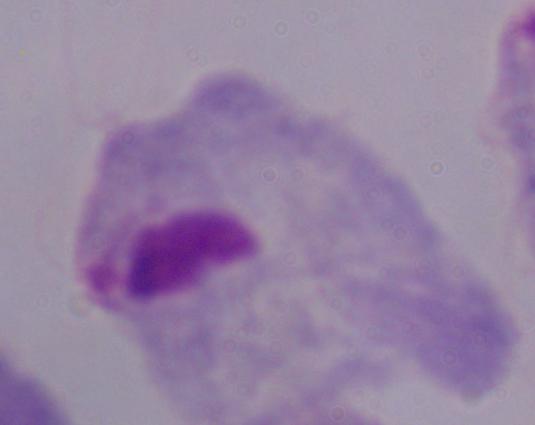

Summary:
  - Magnification: 1000x
  - Modality: photomicrograph
  - Identification: trichomonad